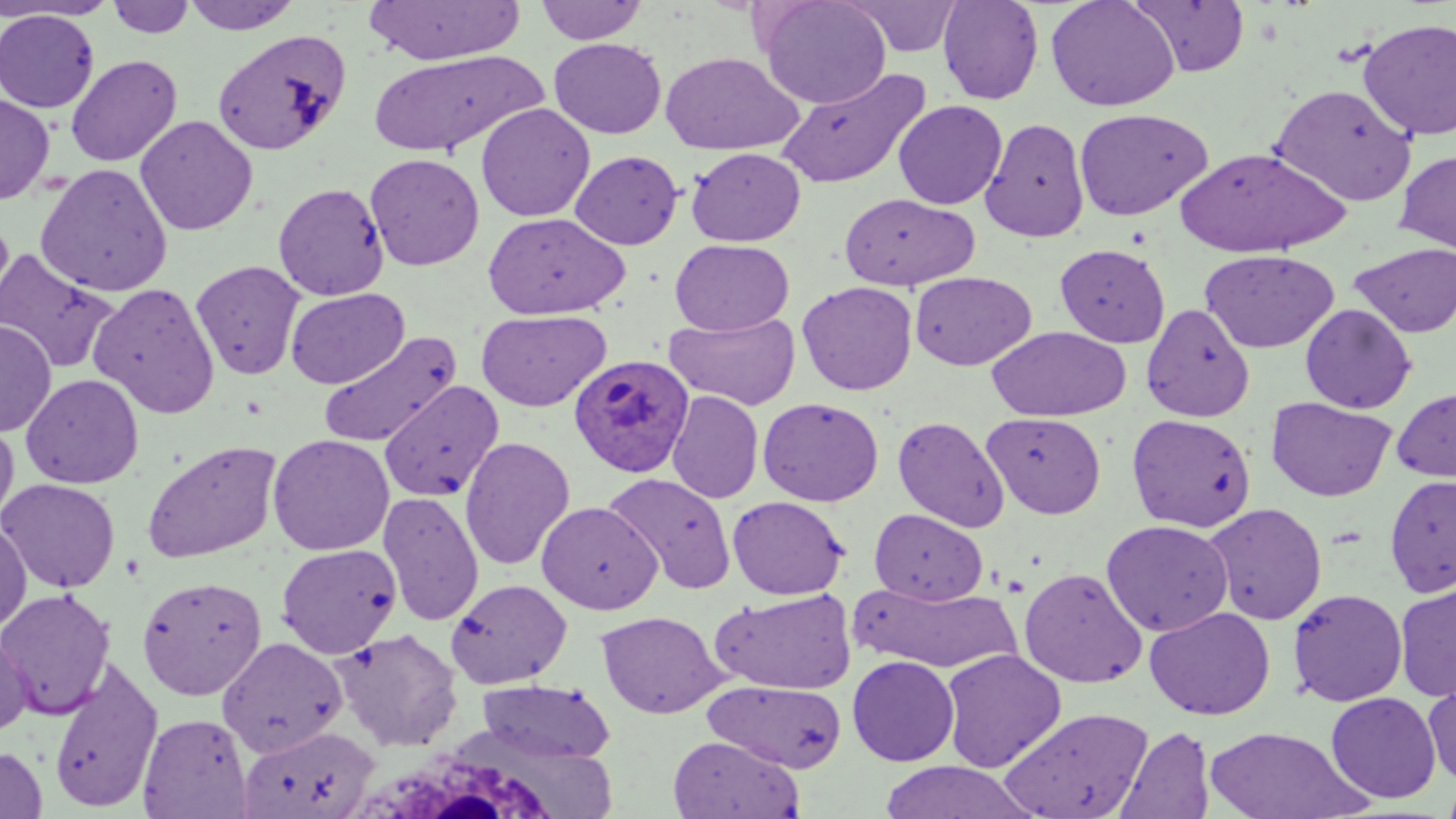

slide-level diagnosis = Plasmodium ovale
image size = 1456×819 pixels
preparation = thin blood smear
Plasmodium ovale-infected red blood cell locations = approximate bounding boxes as named x1/y1/x2/y2 corners in pixels: (x1=570, y1=354, x2=695, y2=478)
magnification = 1000x
modality = light microscopy
white blood cell locations = approximate bounding boxes as named x1/y1/x2/y2 corners in pixels: (x1=358, y1=751, x2=560, y2=818)
stain = May-Grünwald-Giemsa
uninfected red blood cell locations = approximate bounding boxes as named x1/y1/x2/y2 corners in pixels: (x1=1, y1=0, x2=119, y2=21), (x1=107, y1=0, x2=196, y2=39), (x1=181, y1=0, x2=303, y2=34), (x1=363, y1=0, x2=526, y2=65), (x1=756, y1=0, x2=891, y2=109), (x1=842, y1=0, x2=964, y2=58), (x1=937, y1=0, x2=1044, y2=105), (x1=1045, y1=0, x2=1180, y2=112), (x1=1130, y1=0, x2=1251, y2=77), (x1=535, y1=1, x2=649, y2=45), (x1=1, y1=10, x2=100, y2=112), (x1=1357, y1=17, x2=1456, y2=142), (x1=213, y1=29, x2=352, y2=156), (x1=548, y1=37, x2=666, y2=139), (x1=368, y1=49, x2=543, y2=158), (x1=659, y1=52, x2=803, y2=155), (x1=65, y1=54, x2=182, y2=167), (x1=775, y1=68, x2=931, y2=190), (x1=1268, y1=83, x2=1417, y2=207), (x1=0, y1=93, x2=55, y2=205), (x1=893, y1=99, x2=1007, y2=210), (x1=475, y1=103, x2=595, y2=222), (x1=1074, y1=108, x2=1213, y2=221), (x1=134, y1=115, x2=258, y2=235), (x1=980, y1=117, x2=1090, y2=242), (x1=1173, y1=146, x2=1349, y2=258), (x1=685, y1=147, x2=806, y2=247), (x1=1394, y1=149, x2=1456, y2=254), (x1=569, y1=150, x2=684, y2=250), (x1=365, y1=153, x2=484, y2=271), (x1=34, y1=162, x2=173, y2=297), (x1=273, y1=182, x2=390, y2=300), (x1=838, y1=192, x2=979, y2=291), (x1=482, y1=212, x2=631, y2=320), (x1=669, y1=238, x2=795, y2=336), (x1=1349, y1=242, x2=1455, y2=337), (x1=1054, y1=243, x2=1171, y2=348), (x1=0, y1=247, x2=120, y2=374), (x1=1200, y1=249, x2=1340, y2=353), (x1=190, y1=260, x2=306, y2=380), (x1=909, y1=271, x2=1037, y2=371), (x1=797, y1=281, x2=918, y2=395), (x1=88, y1=282, x2=220, y2=420), (x1=285, y1=288, x2=410, y2=389), (x1=1141, y1=302, x2=1255, y2=422), (x1=1300, y1=304, x2=1417, y2=413), (x1=475, y1=309, x2=612, y2=412), (x1=664, y1=311, x2=800, y2=410), (x1=0, y1=320, x2=57, y2=437), (x1=987, y1=326, x2=1131, y2=421), (x1=317, y1=330, x2=462, y2=448), (x1=20, y1=373, x2=144, y2=489), (x1=380, y1=381, x2=504, y2=503), (x1=1392, y1=386, x2=1456, y2=483), (x1=666, y1=390, x2=764, y2=504), (x1=757, y1=396, x2=884, y2=506), (x1=1265, y1=396, x2=1396, y2=502), (x1=983, y1=412, x2=1106, y2=519), (x1=1126, y1=413, x2=1257, y2=533), (x1=893, y1=415, x2=1009, y2=533), (x1=0, y1=417, x2=19, y2=528), (x1=267, y1=434, x2=394, y2=555), (x1=458, y1=436, x2=576, y2=570), (x1=141, y1=439, x2=283, y2=564), (x1=603, y1=472, x2=737, y2=594), (x1=1384, y1=474, x2=1456, y2=597), (x1=0, y1=478, x2=120, y2=593), (x1=377, y1=491, x2=485, y2=626), (x1=727, y1=495, x2=849, y2=600), (x1=536, y1=501, x2=662, y2=614), (x1=1202, y1=503, x2=1328, y2=625), (x1=869, y1=507, x2=989, y2=604), (x1=0, y1=516, x2=31, y2=634), (x1=1100, y1=519, x2=1234, y2=636), (x1=276, y1=543, x2=402, y2=658), (x1=1018, y1=567, x2=1148, y2=689), (x1=136, y1=575, x2=267, y2=700), (x1=445, y1=578, x2=572, y2=688), (x1=852, y1=581, x2=1023, y2=673), (x1=1394, y1=582, x2=1456, y2=702), (x1=0, y1=587, x2=116, y2=720), (x1=1287, y1=587, x2=1408, y2=706), (x1=711, y1=588, x2=857, y2=694), (x1=1144, y1=606, x2=1275, y2=721), (x1=596, y1=610, x2=727, y2=719), (x1=333, y1=627, x2=463, y2=751), (x1=0, y1=628, x2=34, y2=736), (x1=217, y1=636, x2=347, y2=757), (x1=940, y1=648, x2=1066, y2=772), (x1=847, y1=655, x2=960, y2=766), (x1=47, y1=657, x2=165, y2=812), (x1=1422, y1=674, x2=1456, y2=787), (x1=474, y1=679, x2=616, y2=764), (x1=704, y1=679, x2=848, y2=773), (x1=1326, y1=691, x2=1441, y2=803), (x1=998, y1=706, x2=1155, y2=818), (x1=138, y1=713, x2=253, y2=818), (x1=237, y1=726, x2=380, y2=819), (x1=1116, y1=726, x2=1215, y2=819), (x1=1204, y1=726, x2=1369, y2=818), (x1=668, y1=735, x2=802, y2=818), (x1=1, y1=745, x2=48, y2=819), (x1=876, y1=761, x2=1036, y2=818), (x1=1440, y1=775, x2=1456, y2=819)
field of view = one of a larger specimen